Name the parasite shown.
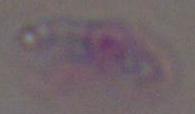
Toxoplasma gondii.

{
  "magnification": "1000x",
  "modality": "micrograph"
}